Locate every Plasmodium parasite.
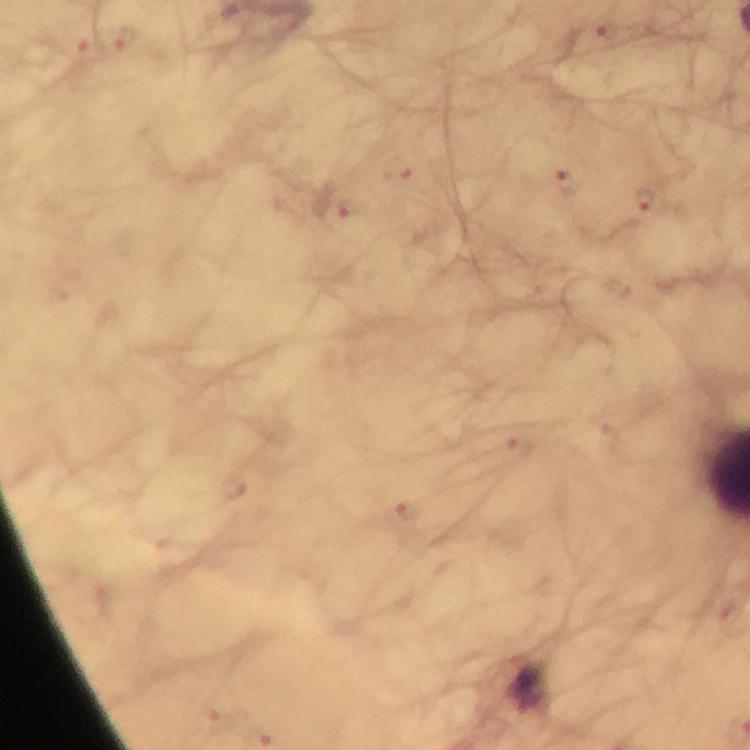
Approximate centers as {x, y} in pixels.
Plasmodium parasites: {597, 35}, {125, 38}, {82, 50}, {398, 168}, {563, 178}, {646, 200}, {345, 207}, {516, 447}, {232, 485}, {407, 511}, {219, 718}.

Summary:
  - Cropped from: one field of view
  - Stain: Giemsa
  - Magnification: 100x
  - Capture: smartphone camera through the microscope
  - Preparation: thick blood film
  - Immersion oil: applied
  - Image size: 750×750 pixels
  - Context: from a diagnostic examination for malaria